Evaluate for Plasmodium parasites.
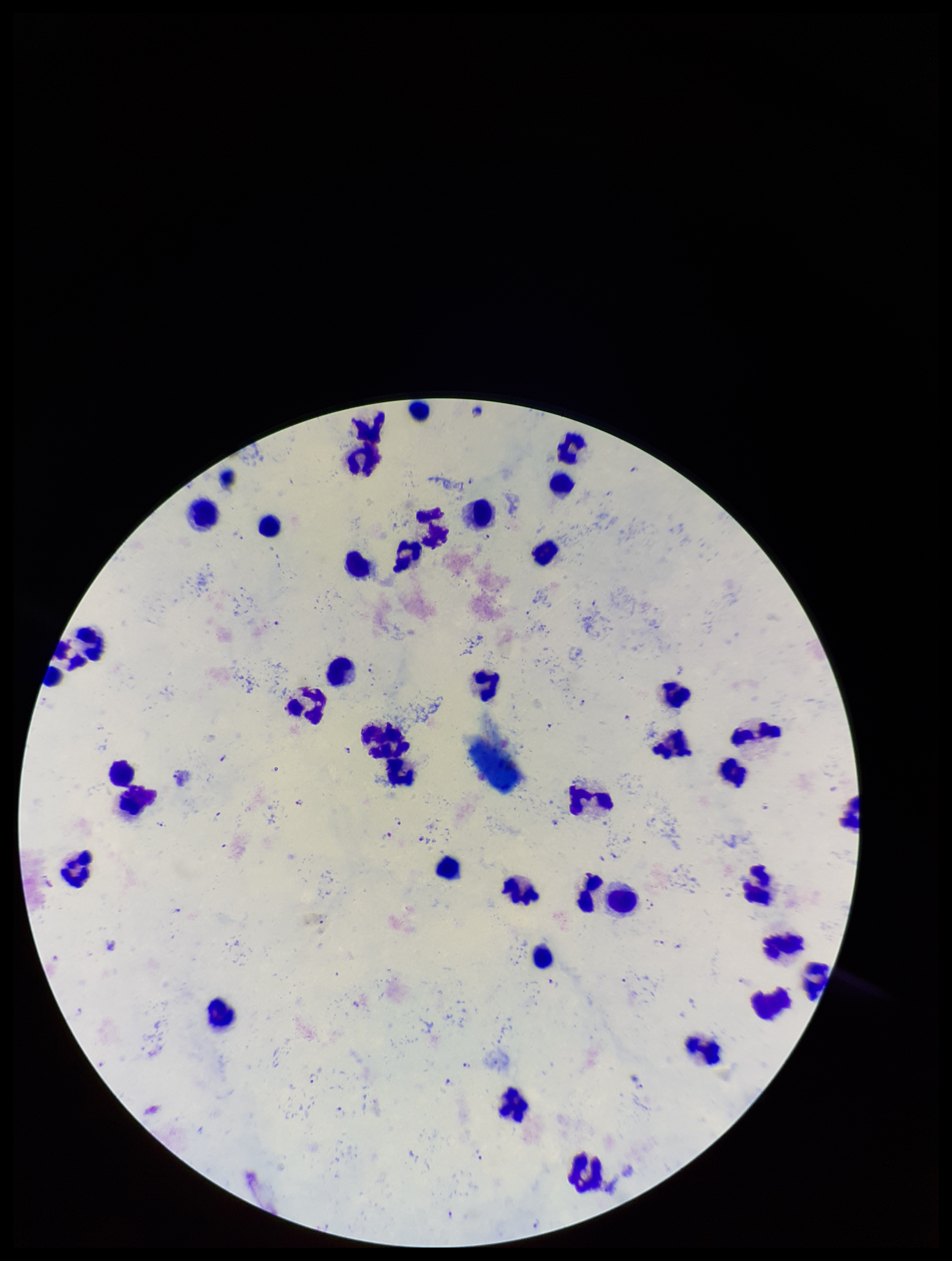

Identified.

{
  "parasite_count": 28,
  "image_size": "952×1261 pixels",
  "preparation": "thick smear",
  "field_of_view": "single",
  "patient_malaria_status": "infected",
  "species_reported_for_this_patient": "Plasmodium falciparum",
  "stain": "Giemsa",
  "capture": "smartphone photograph through the microscope eyepiece",
  "leukocyte_count": 42
}